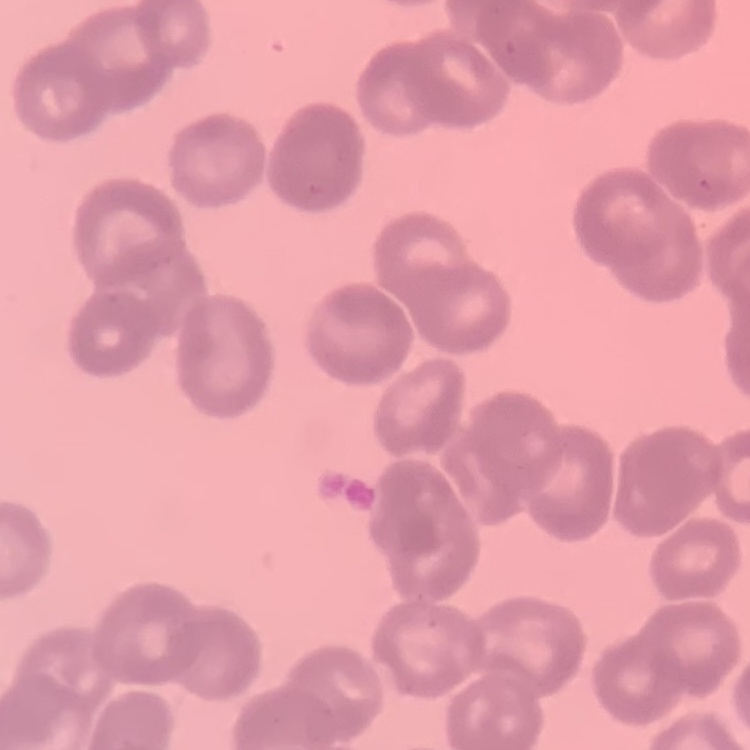

Summary:
  - Red blood cell morphology: rouleaux formation
  - Image type: square crop of a larger photomicrograph
  - Preparation: thin blood smear
  - Stain: Field's or Giemsa